State the blood parasite species.
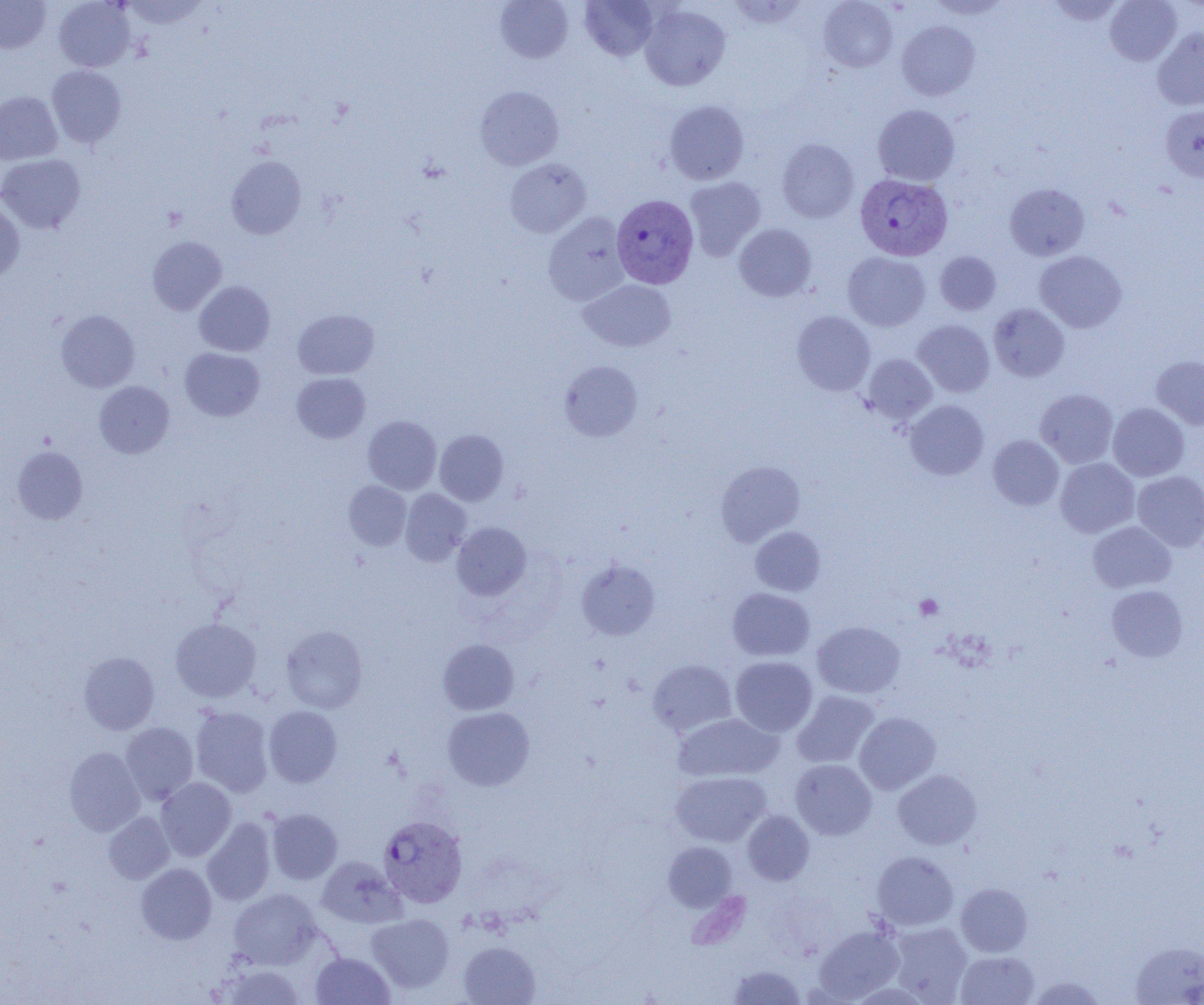

Plasmodium vivax.

Summary:
  - Coordinate format: approximate bounding boxes as [x1, y1, x2, y2] in pixels
  - Platelet locations: [914, 594, 943, 620]
  - Plasmodium vivax-infected red blood cell locations: [855, 174, 952, 261], [611, 195, 699, 289], [377, 814, 467, 908]
  - Uninfected red blood cell locations: [0, 0, 51, 53], [53, 0, 136, 72], [121, 0, 209, 29], [495, 0, 573, 62], [580, 0, 658, 60], [728, 0, 809, 29], [819, 0, 897, 72], [926, 0, 1012, 19], [1046, 0, 1125, 25], [1105, 0, 1182, 65], [640, 4, 730, 91], [897, 21, 980, 100], [1152, 27, 1204, 111], [47, 65, 126, 147], [475, 86, 564, 170], [0, 91, 62, 164], [664, 100, 749, 185], [873, 104, 960, 186], [1160, 105, 1204, 181], [777, 138, 858, 222], [0, 154, 86, 234], [226, 155, 306, 239], [505, 158, 591, 238], [684, 176, 766, 261], [1004, 183, 1089, 260], [0, 201, 25, 282], [543, 212, 630, 305], [734, 224, 817, 301], [147, 236, 227, 315], [935, 251, 1001, 315], [1034, 251, 1126, 332], [843, 252, 930, 331], [579, 279, 676, 352], [194, 281, 275, 356], [988, 303, 1069, 382], [293, 309, 380, 379], [56, 310, 140, 392], [792, 311, 875, 395], [912, 320, 995, 398], [180, 347, 264, 421], [862, 353, 937, 424], [1151, 355, 1204, 431], [559, 361, 643, 441], [292, 373, 371, 443], [94, 381, 174, 458], [1035, 389, 1118, 467], [905, 399, 989, 480], [1108, 403, 1189, 481], [363, 415, 441, 494], [434, 429, 508, 505], [988, 435, 1064, 510], [12, 446, 88, 524], [1055, 458, 1139, 538], [716, 461, 805, 546], [1132, 471, 1204, 551], [343, 481, 411, 550], [400, 488, 471, 566], [1088, 521, 1176, 593], [452, 522, 531, 600], [750, 526, 825, 596], [577, 560, 660, 639], [1107, 585, 1188, 661], [727, 588, 815, 661], [170, 617, 261, 702], [812, 621, 905, 698], [281, 625, 367, 713], [438, 639, 518, 715], [78, 651, 159, 734], [730, 656, 817, 736], [648, 659, 737, 736], [792, 690, 879, 768], [190, 706, 274, 797], [264, 706, 342, 787], [443, 706, 535, 791], [854, 712, 941, 794], [672, 713, 782, 782], [121, 723, 198, 805], [64, 747, 144, 836], [790, 759, 877, 840], [893, 769, 982, 850], [670, 771, 771, 847], [156, 777, 236, 861], [266, 809, 342, 884], [742, 811, 815, 885], [104, 812, 174, 884], [202, 817, 276, 905], [663, 841, 737, 911], [872, 851, 958, 931], [317, 856, 404, 928], [136, 863, 216, 944], [956, 883, 1032, 957], [228, 888, 321, 969], [366, 913, 455, 993], [887, 922, 973, 1004], [814, 925, 904, 1002], [458, 941, 540, 1005], [1131, 942, 1204, 1005], [955, 951, 1039, 1004], [310, 952, 395, 1005], [215, 962, 308, 1005], [728, 965, 806, 1004], [1026, 976, 1109, 1005]
  - Field of view: one of a larger specimen
  - Modality: optical microscopy
  - Magnification: 1000x
  - Preparation: thin blood film
  - Image size: 1204×1005 pixels